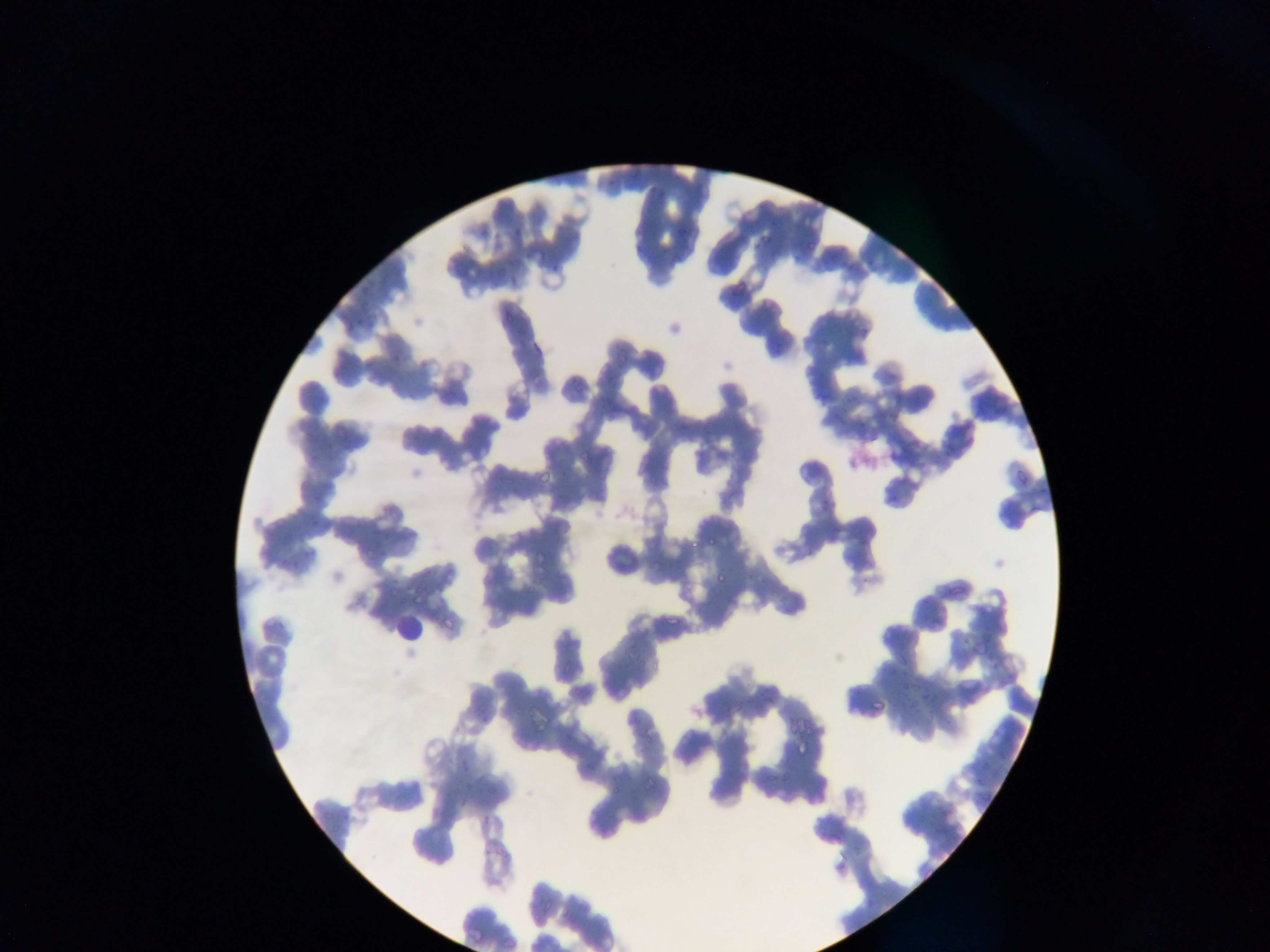
preparation = thin blood film
image size = 1270×952 pixels
capture = mobile-phone photograph through a microscope
field of view = single
country = Ghana
leukocyte locations = approximate bounding boxes as left top right bottom in pixels: 391 612 422 644
malaria parasite locations = approximate bounding boxes as left top right bottom in pixels: 803 237 826 251; 730 272 755 298; 708 533 722 547; 687 537 700 547; 713 568 733 581; 409 590 425 606; 869 690 886 712; 794 741 809 758; 643 769 660 783